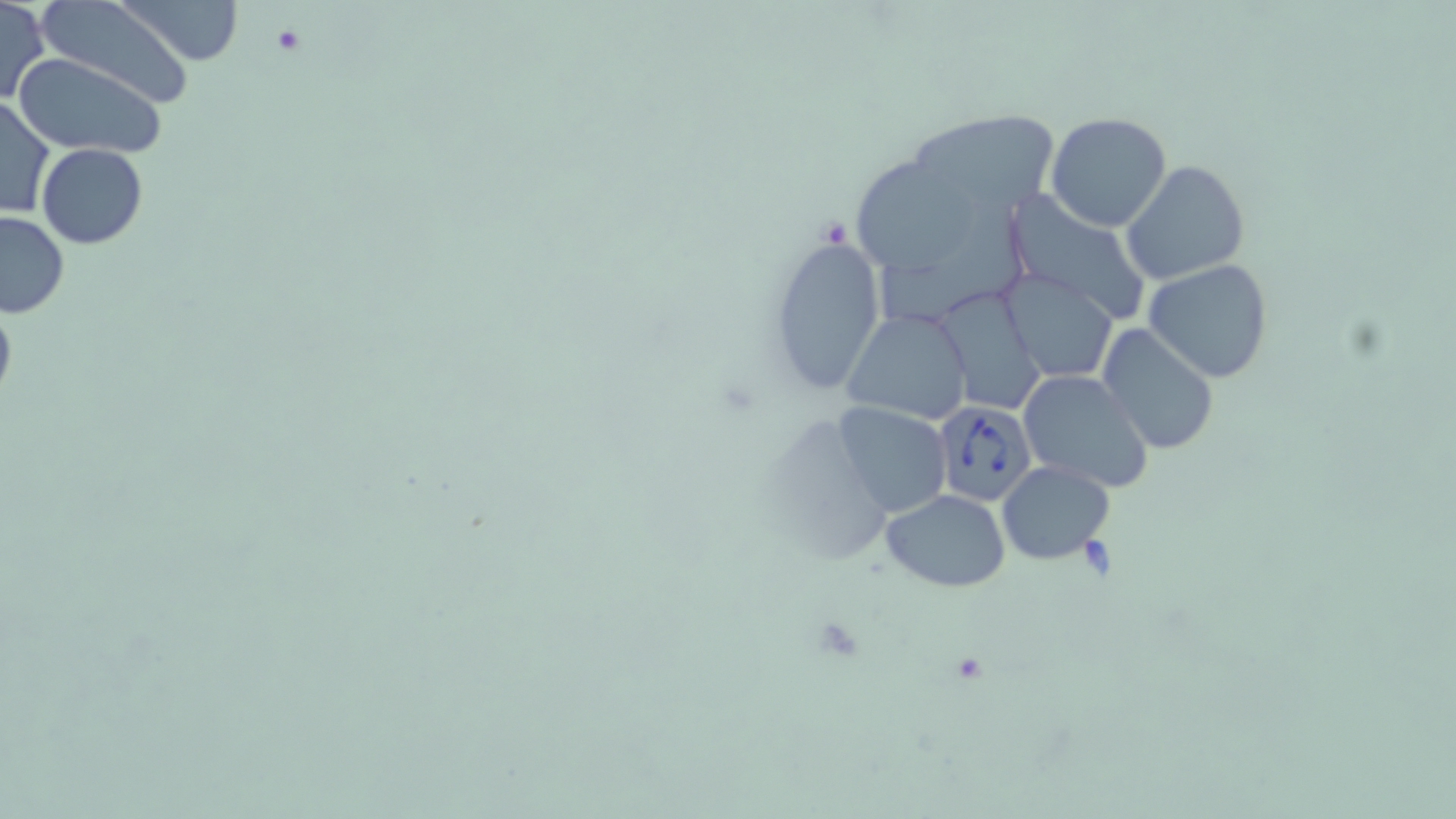

slide-level diagnosis = Babesia divergens
preparation = thin blood film
field of view = one of a larger specimen
image size = 1456×819 pixels
Babesia divergens-infected red blood cell locations = approximate bounding boxes as (x1,y1)-(x2,y2) corner pairs in pixels: (930,400)-(1038,507)
magnification = 1000x
stain = May-Grünwald-Giemsa
uninfected red blood cell locations = approximate bounding boxes as (x1,y1)-(x2,y2) corner pairs in pixels: (118,0)-(242,66), (0,1)-(49,104), (39,1)-(197,109), (14,52)-(167,158), (0,94)-(55,220), (1046,111)-(1172,231), (911,113)-(1068,201), (38,143)-(147,249), (850,155)-(975,277), (1122,161)-(1250,286), (1003,187)-(1148,322), (877,202)-(1028,325), (0,212)-(70,319), (767,234)-(884,394), (1142,259)-(1275,384), (999,269)-(1118,382), (936,282)-(1048,411), (0,299)-(17,412), (843,307)-(973,425), (1097,326)-(1220,456), (1015,371)-(1154,494), (833,402)-(951,518), (998,460)-(1114,565), (882,490)-(1010,590)
platelet locations = approximate bounding boxes as (x1,y1)-(x2,y2) corner pairs in pixels: (270,25)-(306,57)
modality = optical microscopy